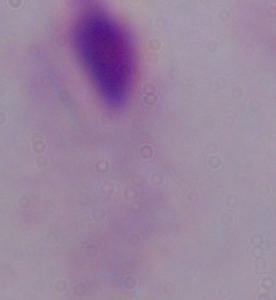

magnification = 1000x
identification = trichomonad
modality = micrograph